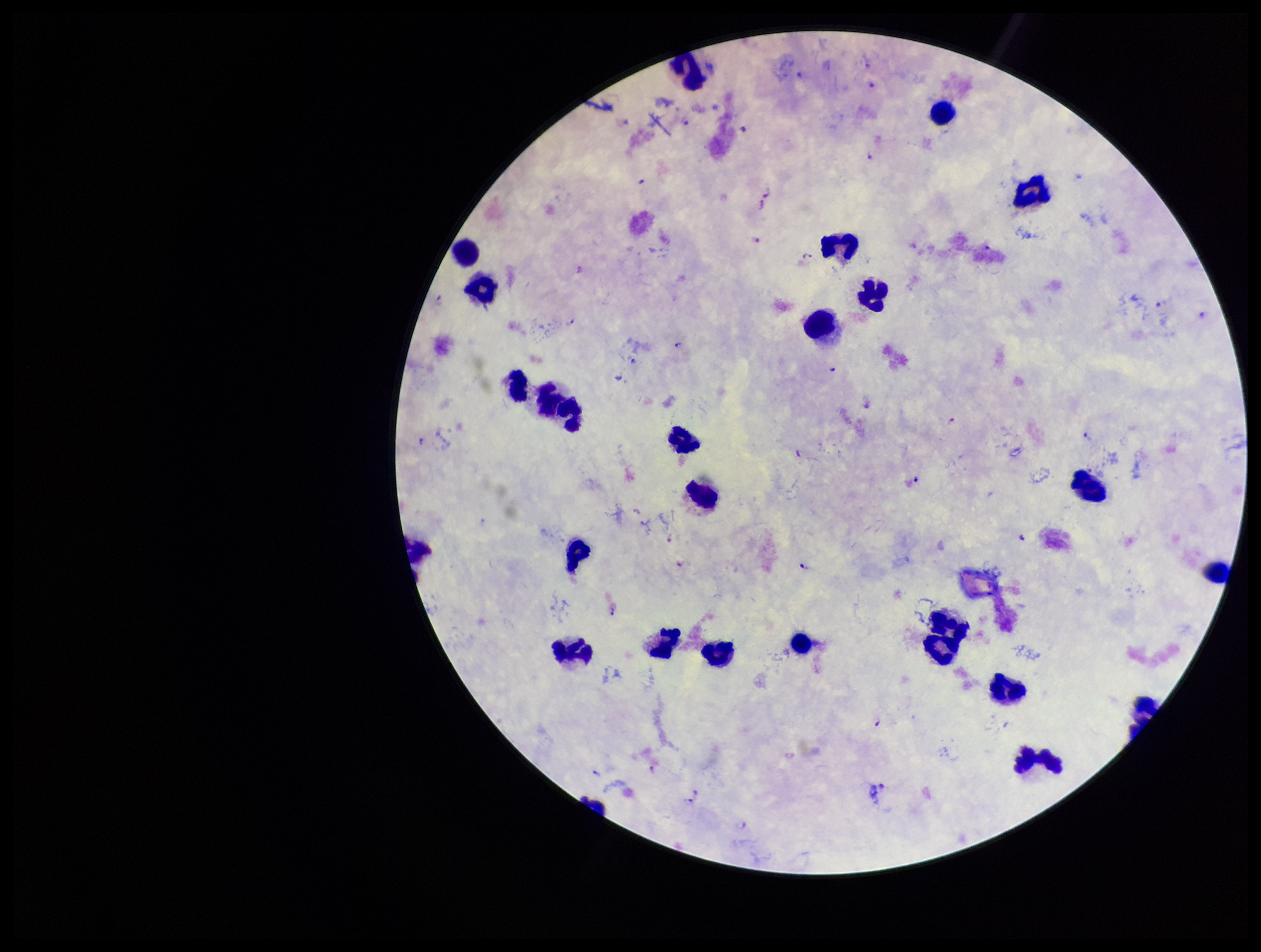 Leukocyte count: 23. Smartphone photograph taken through the eyepiece of a microscope. Parasite count: 24. Patient malaria status: positive. Species reported for this patient: Plasmodium falciparum. One field from this slide. Preparation: thick smear. Plasmodium parasites: seen. Stained with Giemsa. Image is 1261×952 pixels.